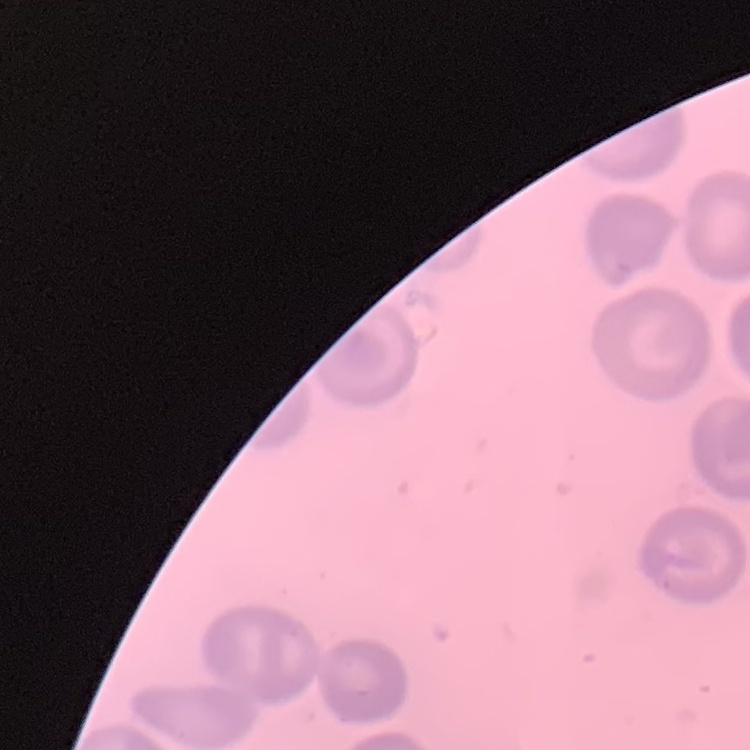
{
  "erythrocyte_morphology": "no rouleaux formation",
  "image_type": "square crop of a larger photomicrograph",
  "preparation": "thin blood film",
  "stain": "Field's or Giemsa"
}